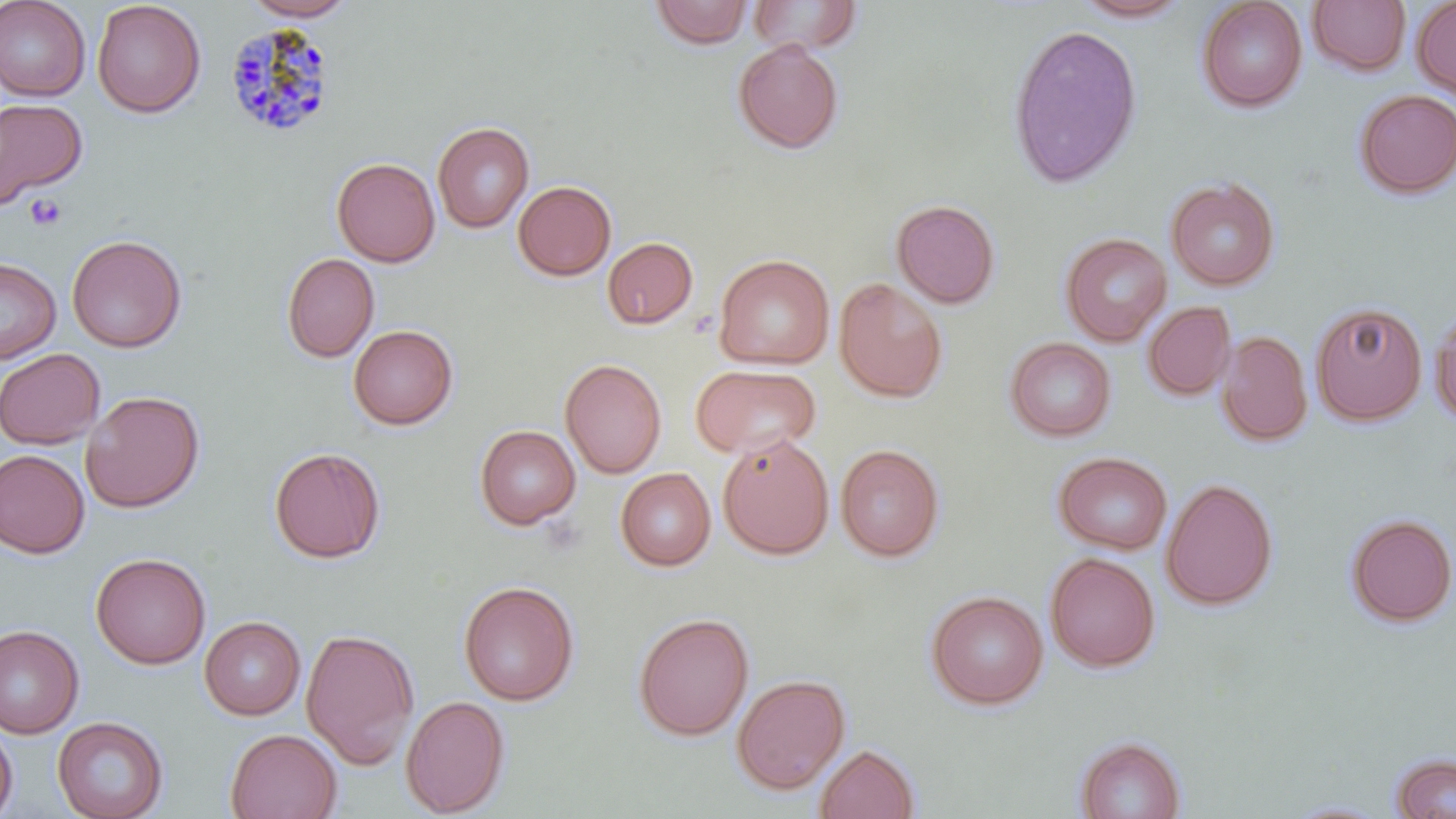
Summary:
  - Coordinate format: approximate bounding boxes as (x1,y1)-(x2,y2) corner pairs in pixels
  - Uninfected red blood cell locations: (0,0)-(91,101), (92,0)-(207,118), (241,0)-(358,21), (747,0)-(864,55), (1071,0)-(1194,23), (1196,0)-(1307,112), (1307,0)-(1411,77), (1411,0)-(1456,102), (649,1)-(752,49), (1007,23)-(1143,188), (732,39)-(844,154), (1354,89)-(1456,199), (0,97)-(87,208), (432,120)-(534,233), (332,157)-(440,267), (1165,176)-(1280,291), (512,180)-(616,281), (891,199)-(1001,309), (1060,231)-(1171,346), (67,234)-(187,353), (602,236)-(699,330), (281,252)-(380,363), (713,253)-(835,370), (0,256)-(61,364), (834,278)-(948,403), (1143,301)-(1236,401), (1310,301)-(1428,425), (1430,304)-(1456,428), (347,324)-(459,430), (1215,330)-(1313,447), (1005,336)-(1116,441), (0,348)-(105,449), (560,358)-(667,478), (690,364)-(821,459), (81,390)-(205,513), (474,425)-(581,530), (717,433)-(834,560), (835,443)-(944,562), (268,446)-(386,563), (0,449)-(90,558), (1053,451)-(1173,555), (615,467)-(716,571), (1160,478)-(1278,611), (1345,513)-(1456,627), (90,552)-(211,669), (1044,552)-(1160,673), (459,580)-(579,706), (926,590)-(1048,710), (633,612)-(754,741), (199,616)-(305,720), (0,625)-(84,739), (301,627)-(419,769), (731,674)-(850,795), (400,695)-(510,816), (52,715)-(168,819), (0,720)-(18,818), (225,728)-(343,818), (1074,735)-(1187,819), (814,743)-(920,819), (1390,753)-(1456,818), (1282,799)-(1395,818)
  - Platelet locations: (25,193)-(66,231)
  - Plasmodium malariae-infected red blood cell locations: (224,22)-(337,138)
  - Slide-level diagnosis: Plasmodium malariae
  - Field of view: one of a larger specimen
  - Image size: 1456×819 pixels
  - Preparation: thin blood film
  - Magnification: 1000x
  - Modality: light microscopy
  - Stain: May-Grünwald-Giemsa